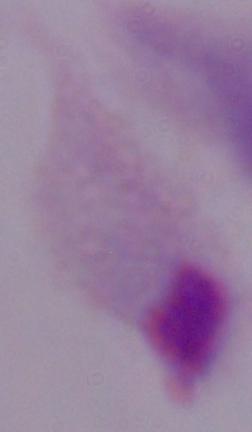 Photomicrograph. Captured at 1000x magnification. A trichomonad is shown.